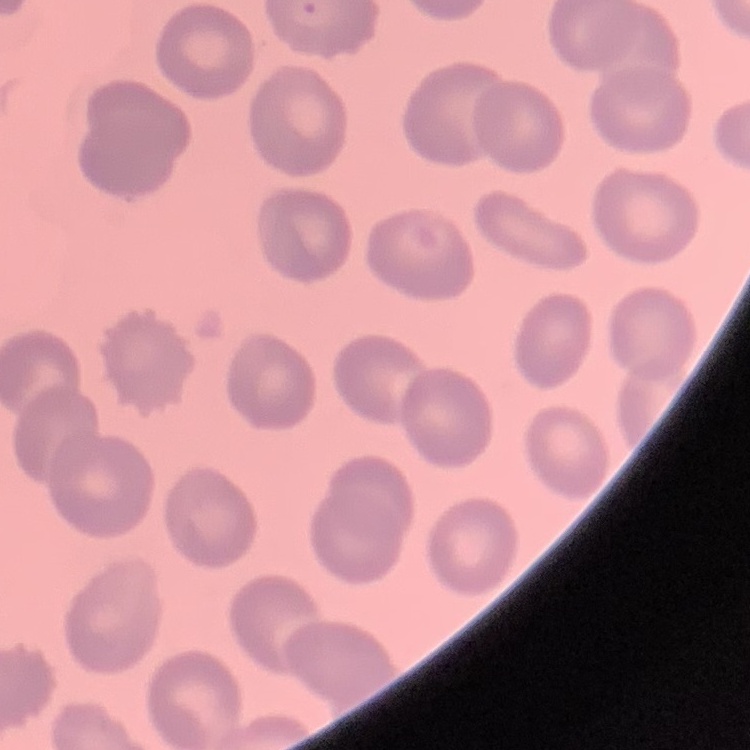
Summary:
  - Red blood cell morphology: no rouleaux formation
  - Preparation: thin blood smear
  - Image type: square crop of a larger photomicrograph
  - Stain: Field's or Giemsa